Name the parasite shown.
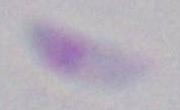

Toxoplasma gondii.

Summary:
  - Modality: photomicrograph
  - Magnification: 1000x